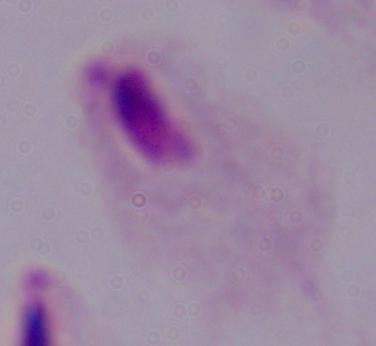

Summary:
  - Magnification: 1000x
  - Identification: trichomonad
  - Modality: photomicrograph